Assess the morphology of the red blood cells.
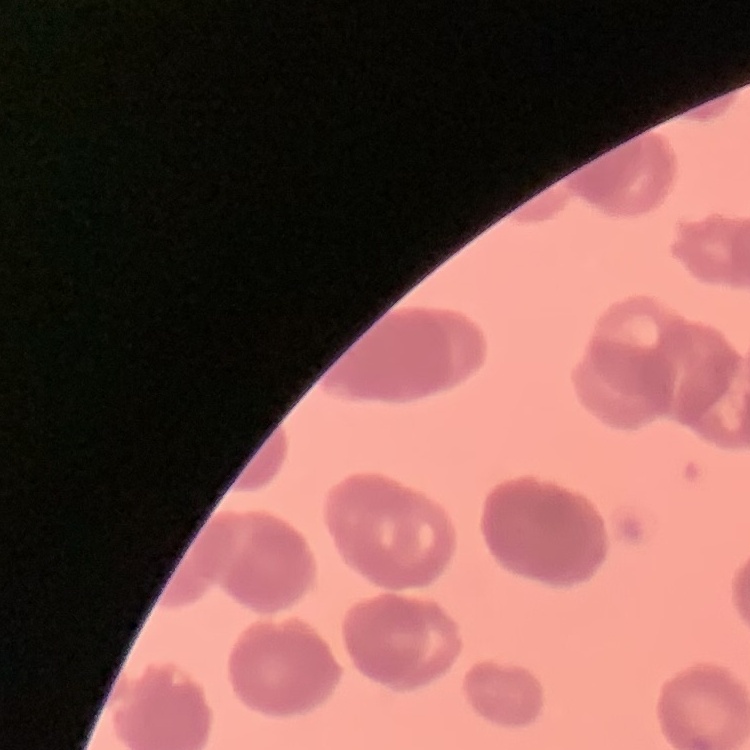
Rouleaux formation.

stain = Field's or Giemsa
image type = square crop of a larger photomicrograph
preparation = thin peripheral smear